Mark where platelets are.
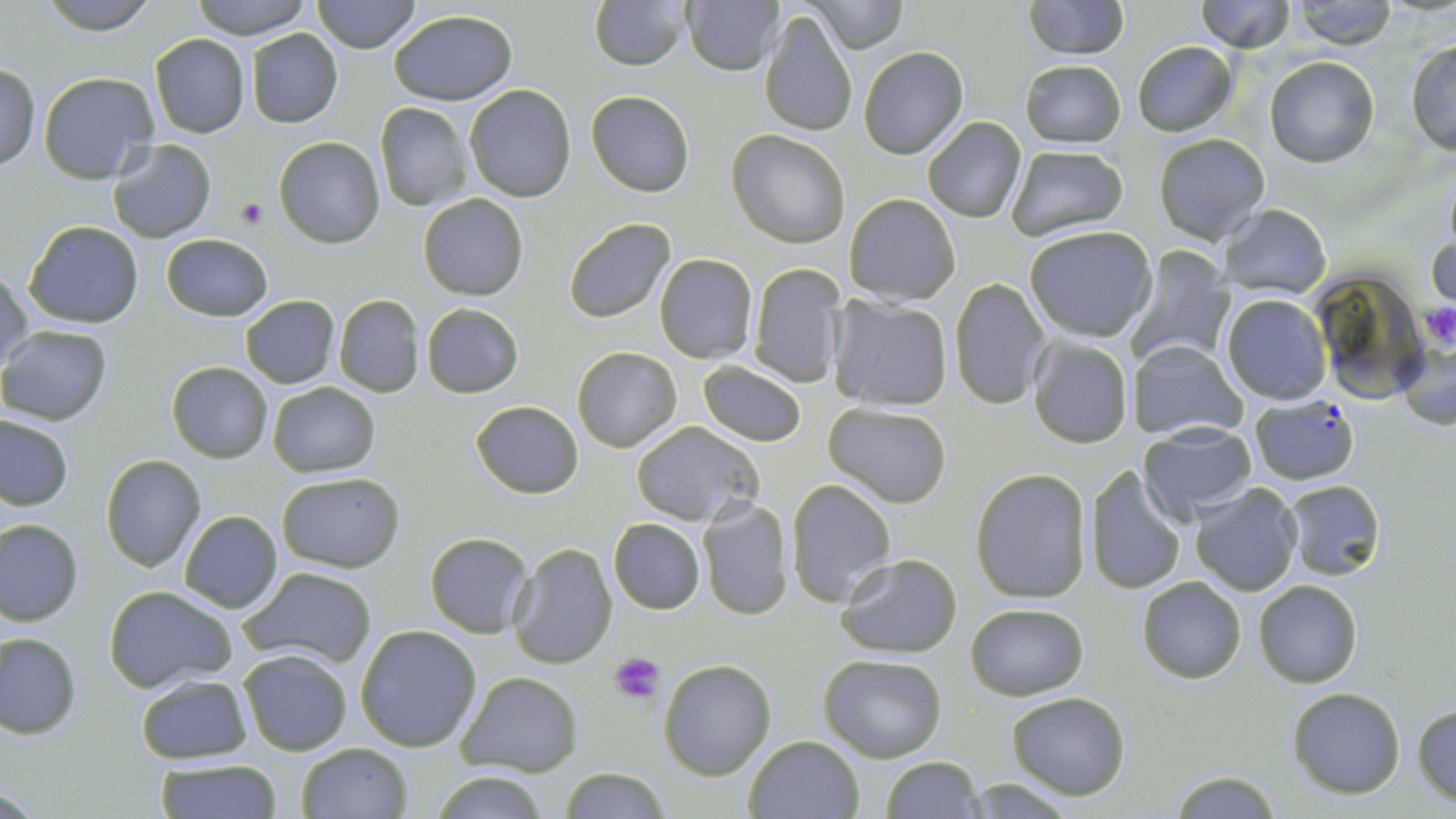

Approximate bounding boxes as [x1, y1, x2, y2] in pixels.
Platelets: [236, 196, 268, 228], [1423, 304, 1456, 349], [611, 652, 666, 701].

plasmodium_falciparum_infected_red_blood_cell_locations: 'approximate bounding boxes as [x1, y1, x2, y2] in pixels: [1250, 394, 1360, 484]'
slide_level_diagnosis: Plasmodium falciparum
uninfected_red_blood_cell_locations: 'approximate bounding boxes as [x1, y1, x2, y2] in pixels: [38, 0, 160, 33], [187, 0, 315, 40], [312, 0, 419, 52], [589, 0, 689, 71], [1022, 0, 1128, 58], [683, 1, 784, 76], [807, 1, 906, 53], [1194, 1, 1293, 52], [1292, 1, 1397, 49], [388, 9, 517, 106], [759, 9, 858, 138], [244, 28, 344, 128], [149, 34, 251, 138], [1406, 38, 1456, 157], [1130, 40, 1239, 136], [858, 46, 968, 158], [1265, 55, 1378, 167], [1020, 59, 1125, 148], [0, 63, 41, 171], [40, 72, 160, 184], [465, 83, 576, 202], [586, 90, 697, 197], [373, 102, 473, 211], [921, 117, 1027, 223], [728, 131, 850, 247], [1153, 133, 1269, 244], [274, 136, 386, 249], [107, 140, 217, 242], [1006, 144, 1128, 241], [418, 193, 528, 301], [845, 193, 961, 305], [1218, 203, 1332, 299], [563, 216, 676, 324], [24, 220, 143, 329], [1024, 225, 1156, 343], [1430, 229, 1455, 310], [161, 234, 272, 322], [1127, 246, 1234, 367], [654, 253, 758, 364], [747, 262, 847, 388], [1, 268, 34, 374], [1309, 270, 1430, 403], [949, 278, 1052, 410], [333, 293, 424, 397], [1222, 294, 1331, 405], [239, 295, 340, 388], [829, 296, 954, 413], [421, 303, 524, 398], [0, 325, 112, 424], [1396, 335, 1455, 430], [1027, 336, 1134, 450], [1129, 341, 1248, 442], [573, 347, 681, 451], [167, 361, 273, 464], [696, 361, 809, 446], [267, 382, 379, 477], [471, 400, 583, 498], [825, 403, 952, 506], [0, 414, 74, 512], [630, 421, 763, 526], [1138, 422, 1257, 523], [100, 454, 206, 571], [1083, 467, 1188, 595], [969, 470, 1091, 602], [277, 471, 405, 573], [786, 478, 897, 609], [1282, 480, 1385, 580], [1190, 483, 1304, 598], [695, 497, 793, 621], [178, 510, 283, 613], [0, 517, 83, 625], [609, 518, 706, 614], [425, 532, 534, 637], [507, 542, 618, 669], [833, 553, 963, 659], [239, 565, 377, 668], [1137, 576, 1248, 683], [1254, 579, 1362, 687], [104, 585, 236, 693], [965, 603, 1089, 699], [355, 624, 483, 752], [0, 633, 81, 738], [238, 648, 353, 756], [819, 652, 947, 763], [659, 658, 777, 780], [457, 671, 583, 775], [134, 674, 253, 764], [1286, 687, 1405, 798], [1006, 691, 1130, 800], [1412, 704, 1456, 805], [744, 734, 865, 819], [296, 741, 413, 819], [882, 756, 982, 819], [153, 760, 283, 818], [561, 766, 669, 819], [428, 769, 552, 819], [1170, 772, 1279, 818]'
field_of_view: single
magnification: 1000x
image_size: 1456×819 pixels
preparation: thin blood film
stain: May-Grünwald-Giemsa
modality: optical microscopy